Locate and identify every blood parasite.
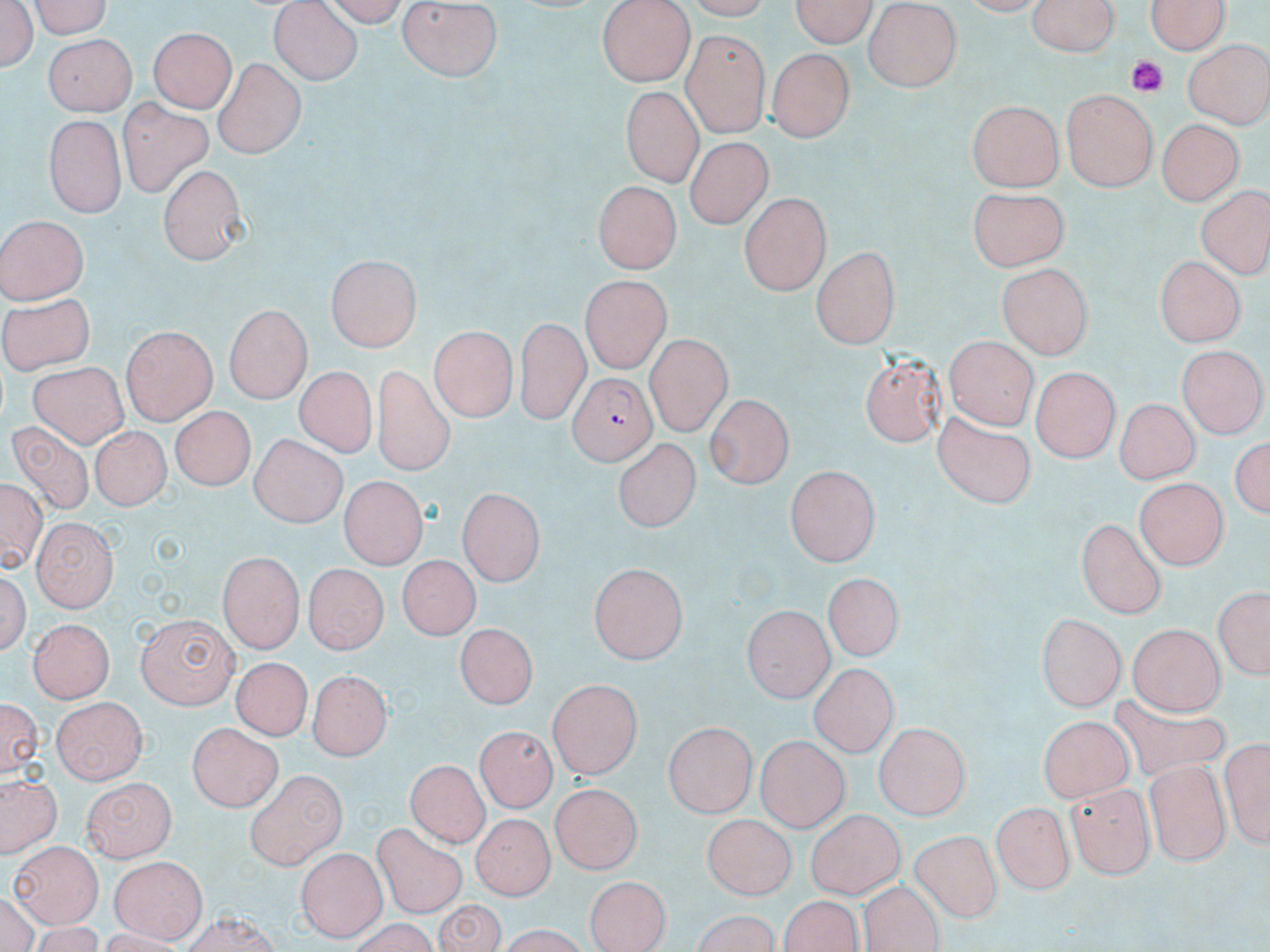

Approximate bounding boxes as (x1, y1, x2, y2) in pixels.
Plasmodium falciparum-infected red blood cells: (566, 371, 653, 464).
No Plasmodium ovale, Plasmodium malariae, Plasmodium vivax, Babesia divergens, or Trypanosoma brucei observed.

slide-level diagnosis = Plasmodium falciparum
preparation = thin blood smear
magnification = 1000x
image size = 1270×952 pixels
platelet locations = approximate bounding boxes as (x1, y1, x2, y2) in pixels: (1126, 56, 1165, 95)
field of view = one of a larger specimen
modality = optical microscopy
stain = May-Grünwald-Giemsa
uninfected red blood cell locations = approximate bounding boxes as (x1, y1, x2, y2) in pixels: (0, 0, 38, 72), (24, 0, 118, 37), (322, 0, 413, 24), (598, 0, 694, 85), (785, 0, 880, 49), (1025, 0, 1120, 58), (1144, 0, 1232, 56), (268, 2, 362, 85), (395, 2, 507, 83), (860, 5, 964, 88), (31, 20, 137, 79), (148, 24, 237, 111), (681, 32, 771, 136), (43, 34, 136, 114), (1185, 39, 1270, 125), (770, 48, 856, 140), (214, 59, 303, 157), (619, 85, 702, 185), (1061, 90, 1158, 192), (117, 98, 215, 201), (966, 100, 1062, 191), (41, 114, 122, 218), (1153, 118, 1241, 206), (682, 129, 772, 223), (157, 164, 248, 263), (590, 179, 678, 270), (965, 185, 1067, 270), (1199, 189, 1268, 279), (739, 191, 829, 291), (0, 216, 87, 303), (812, 247, 903, 349), (325, 254, 420, 349), (1151, 257, 1249, 344), (998, 262, 1093, 357), (581, 276, 669, 373), (0, 284, 97, 378), (226, 305, 312, 404), (515, 320, 588, 420), (428, 326, 516, 421), (121, 327, 216, 424), (645, 334, 733, 434), (943, 337, 1033, 428), (1178, 346, 1265, 435), (861, 353, 946, 443), (26, 359, 129, 443), (1035, 364, 1124, 458), (374, 366, 450, 474), (292, 367, 378, 456), (701, 393, 792, 490), (1116, 399, 1199, 483), (167, 406, 255, 490), (926, 411, 1038, 509), (7, 419, 97, 512), (87, 420, 171, 506), (1231, 432, 1270, 525), (249, 434, 347, 525), (611, 437, 699, 535), (787, 466, 878, 565), (337, 479, 428, 570), (1134, 479, 1227, 569), (460, 485, 544, 580), (33, 518, 117, 610), (1078, 519, 1167, 618), (214, 552, 302, 653), (394, 555, 480, 645), (302, 564, 387, 653), (588, 564, 686, 666), (820, 575, 906, 660), (1211, 584, 1267, 684), (740, 605, 833, 700), (136, 612, 237, 707), (1038, 612, 1130, 711), (26, 617, 116, 705), (453, 624, 540, 707), (1123, 624, 1226, 718), (233, 654, 311, 737), (811, 663, 897, 755), (312, 666, 391, 759), (548, 676, 644, 777), (3, 695, 43, 778), (52, 698, 143, 784), (1038, 709, 1130, 799), (665, 721, 757, 819), (875, 722, 972, 817), (190, 723, 283, 812), (475, 725, 554, 814), (1222, 732, 1269, 848), (755, 736, 849, 832), (407, 759, 494, 842), (1146, 761, 1232, 864), (244, 771, 344, 869), (81, 776, 177, 862), (3, 778, 58, 857), (1066, 779, 1155, 877), (548, 783, 640, 873), (993, 800, 1075, 895), (470, 808, 549, 897), (805, 810, 906, 898), (703, 813, 796, 898), (375, 826, 470, 916), (908, 830, 1003, 922), (11, 839, 102, 926), (296, 847, 385, 939), (111, 858, 206, 943), (586, 873, 671, 952), (862, 882, 941, 952), (781, 897, 863, 952), (434, 898, 506, 951)